Comment on the morphology of the red blood cells.
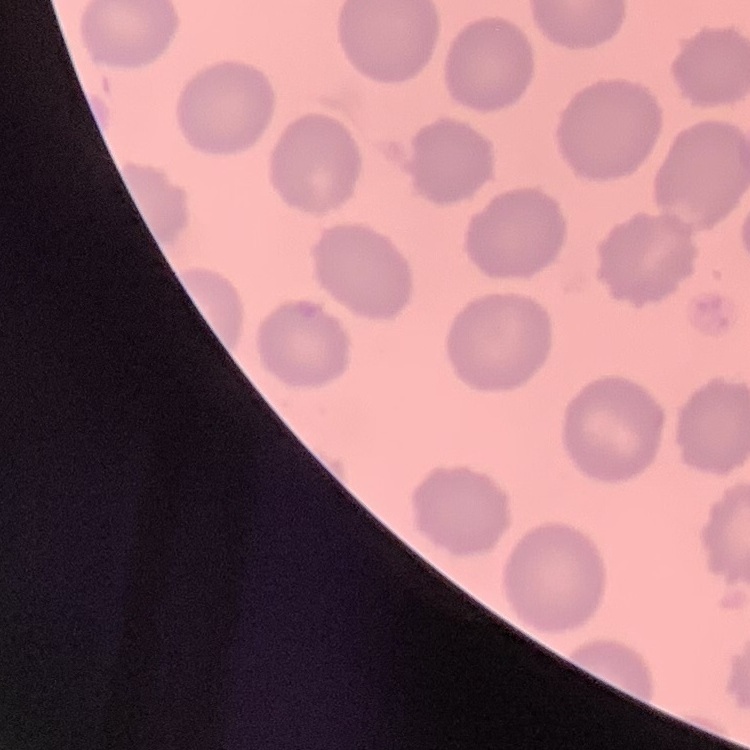

No rouleaux formation.

Summary:
  - Preparation: thin peripheral smear
  - Image type: one tile cut from a larger photomicrograph
  - Stain: Field's or Giemsa